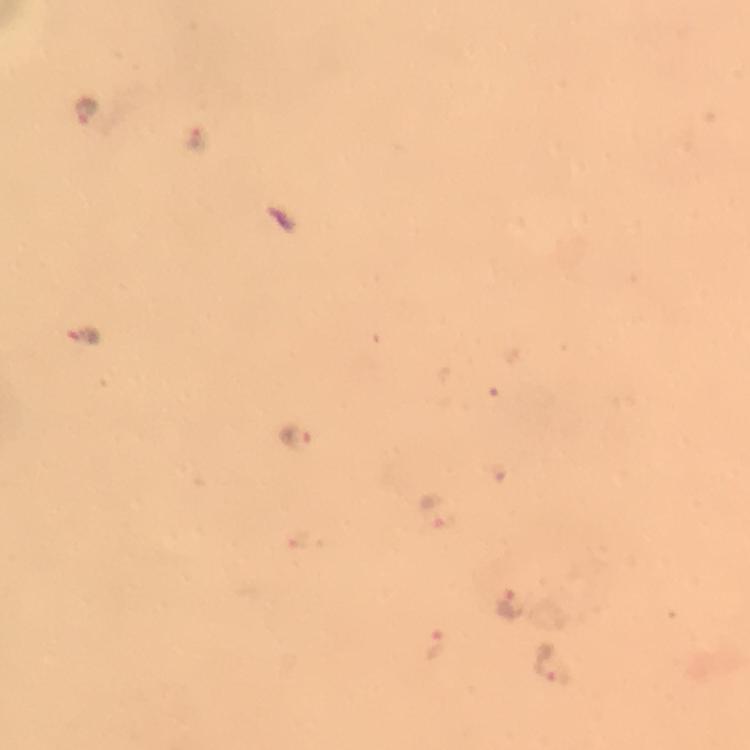 Approximate centers as [x, y] in pixels. Plasmodium parasite locations: [89, 112], [199, 139], [297, 436], [438, 514], [509, 603], [431, 647], [551, 663]. Giemsa-stained preparation. Thick blood film. Image is 750×750 pixels. 100x magnification. Immersion oil was used. A crop from one field of view. From a diagnostic examination for malaria. Photographed through the microscope with a smartphone camera.